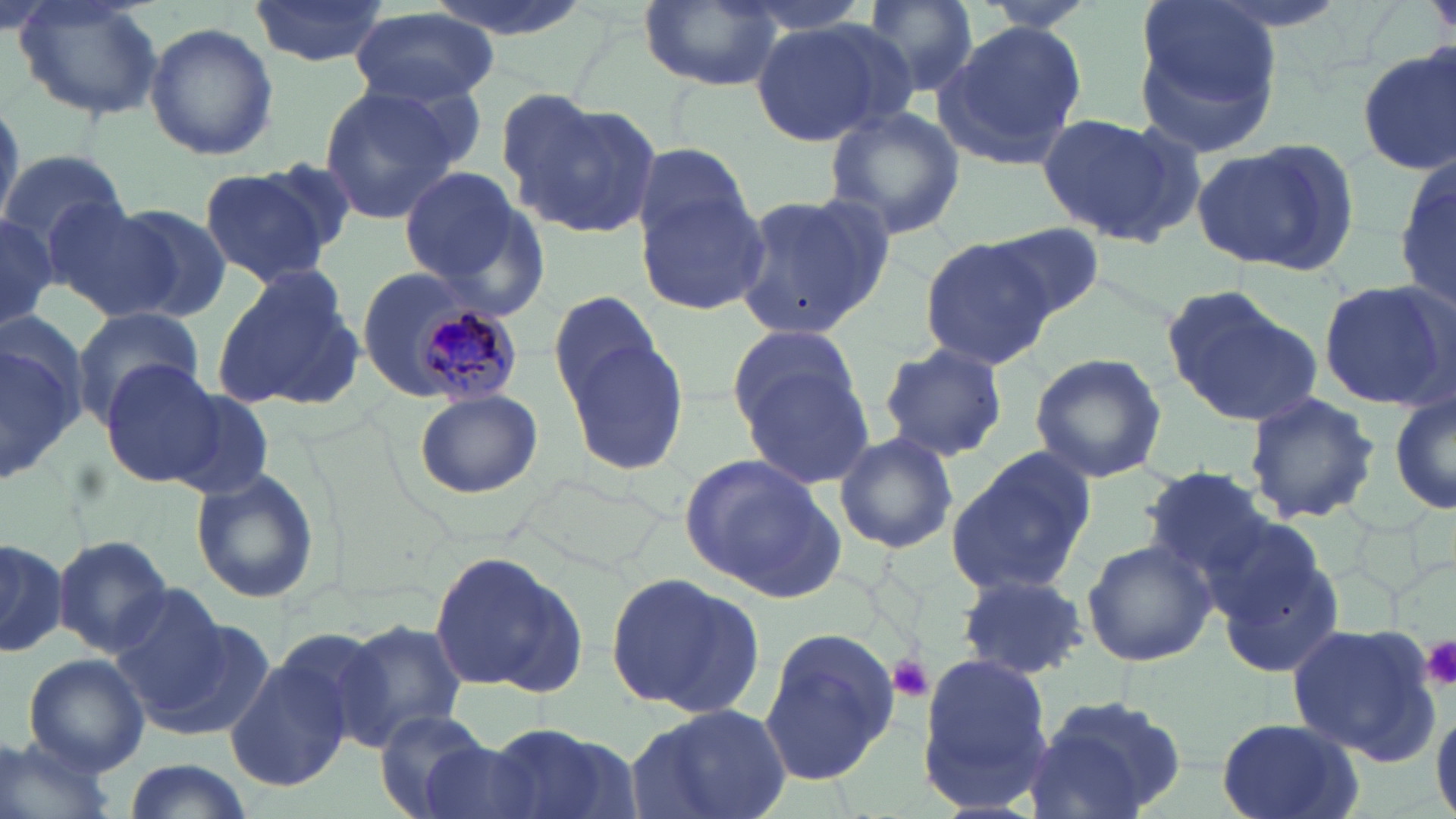
slide_level_diagnosis: Plasmodium malariae
image_size: 1456×819 pixels
preparation: thin blood smear
uninfected_red_blood_cell_locations: 'approximate bounding boxes as [x1, y1, x2, y2] in pixels: [13, 0, 163, 123], [248, 0, 388, 68], [420, 0, 595, 44], [637, 0, 788, 89], [852, 0, 980, 101], [964, 0, 1112, 32], [351, 8, 499, 109], [1130, 17, 1284, 158], [749, 18, 900, 148], [936, 20, 1090, 167], [145, 21, 277, 161], [1356, 48, 1455, 175], [316, 84, 464, 221], [504, 91, 664, 242], [0, 93, 23, 233], [823, 106, 966, 242], [1036, 112, 1201, 249], [1190, 139, 1358, 274], [633, 142, 753, 241], [0, 149, 126, 258], [1396, 150, 1454, 320], [247, 157, 359, 264], [196, 166, 334, 285], [397, 166, 527, 288], [635, 187, 772, 314], [730, 189, 893, 339], [50, 204, 183, 320], [106, 204, 232, 321], [0, 213, 58, 334], [983, 223, 1105, 321], [918, 235, 1056, 370], [360, 268, 442, 402], [211, 269, 364, 412], [1317, 277, 1455, 411], [1162, 285, 1320, 426], [548, 288, 668, 406], [72, 308, 205, 420], [0, 320, 87, 485], [726, 326, 866, 434], [563, 332, 691, 479], [876, 341, 1011, 463], [1028, 352, 1169, 483], [96, 358, 223, 487], [739, 367, 877, 488], [167, 389, 280, 498], [1389, 389, 1456, 517], [413, 391, 543, 498], [1243, 391, 1382, 523], [834, 432, 959, 555], [945, 445, 1098, 595], [678, 454, 838, 596], [189, 465, 321, 605], [1137, 465, 1288, 586], [50, 533, 177, 656], [0, 535, 66, 656], [1082, 539, 1217, 669], [428, 550, 583, 695], [1217, 552, 1347, 678], [604, 569, 764, 717], [955, 570, 1091, 679], [105, 591, 255, 732], [337, 619, 471, 749], [269, 622, 403, 754], [758, 623, 902, 790], [1289, 624, 1440, 764], [223, 648, 358, 792], [22, 652, 150, 776], [916, 654, 1056, 809], [1021, 693, 1191, 817], [626, 704, 792, 819], [1432, 704, 1456, 819], [375, 708, 493, 817], [1215, 719, 1363, 819], [486, 722, 637, 819], [0, 732, 122, 819], [416, 738, 548, 819], [119, 761, 257, 819]'
field_of_view: single
magnification: 1000x
platelet_locations: 'approximate bounding boxes as [x1, y1, x2, y2] in pixels: [1422, 636, 1456, 687], [886, 652, 936, 702]'
plasmodium_malariae_infected_red_blood_cell_locations: 'approximate bounding boxes as [x1, y1, x2, y2] in pixels: [408, 297, 523, 409]'
stain: May-Grünwald-Giemsa
modality: light microscopy